Comment on the morphology of the erythrocytes.
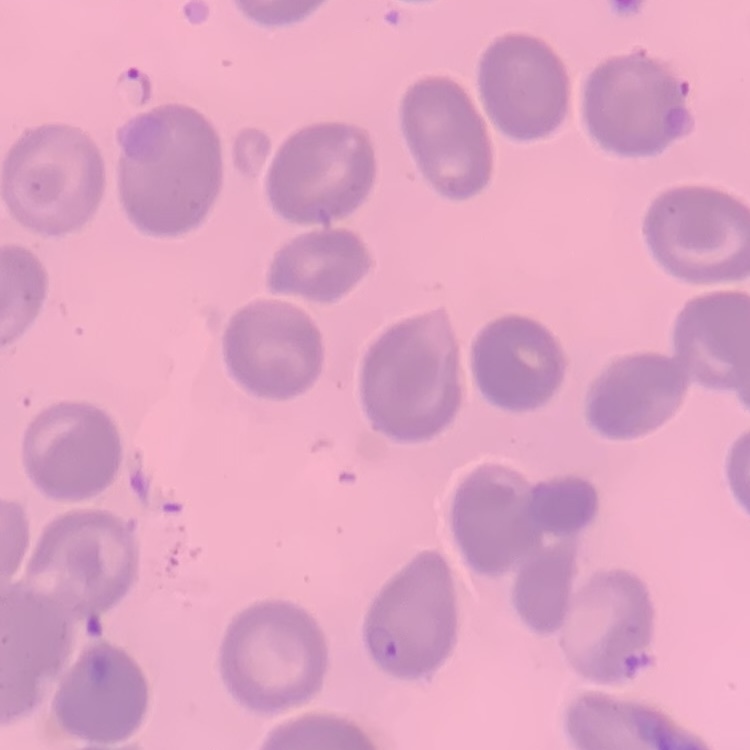

They show no rouleaux formation.

preparation = thin peripheral smear
stain = Field's or Giemsa
image type = square crop of a larger photomicrograph